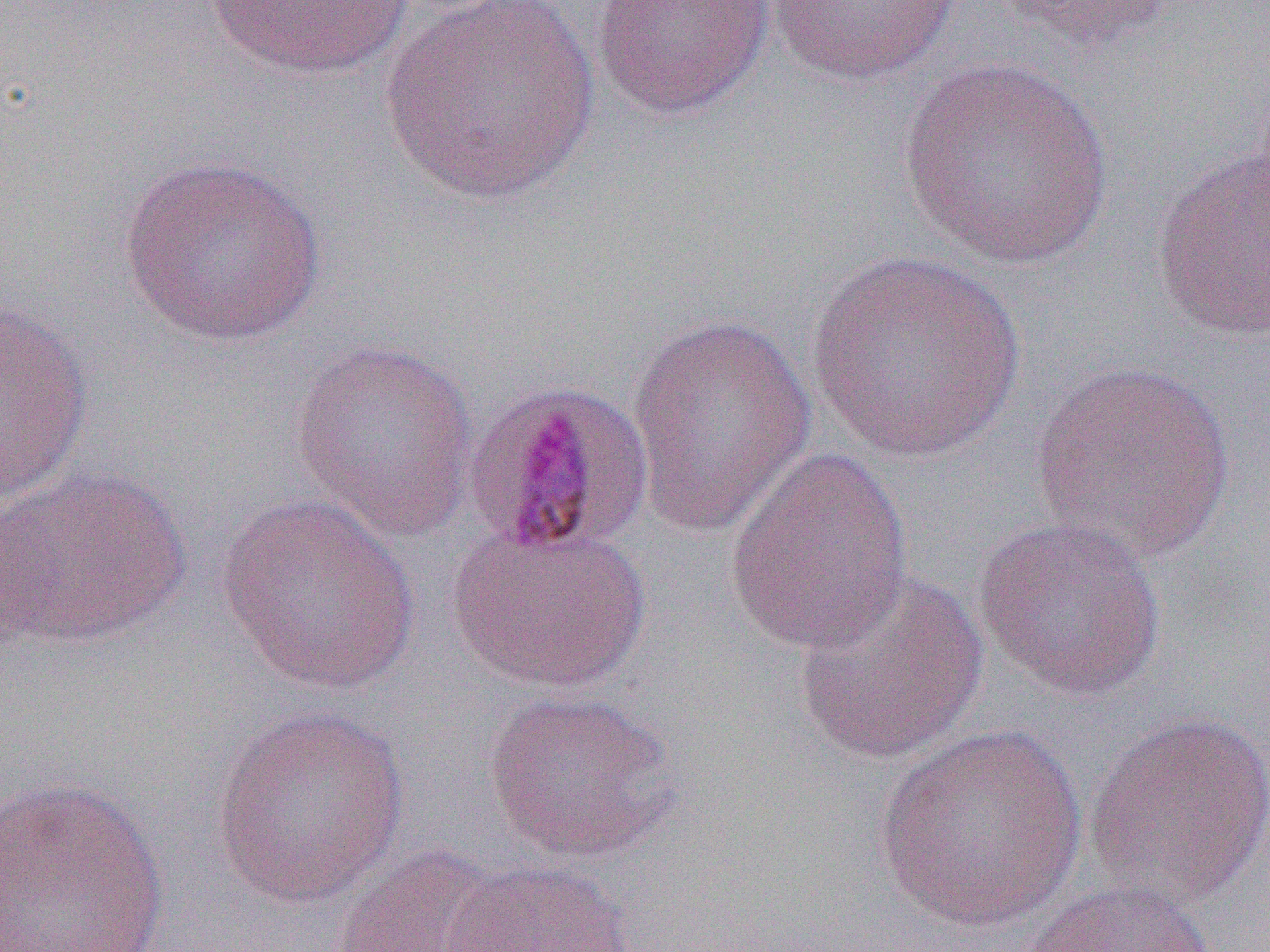
Summary:
  - Coordinate format: approximate bounding boxes as (x1,y1)-(x2,y2) corner pairs in pixels
  - Uninfected red blood cell locations: (202,0)-(420,80), (590,0)-(775,122), (986,0)-(1181,52), (377,1)-(602,205), (767,1)-(961,85), (895,57)-(1118,272), (1150,144)-(1269,342), (117,153)-(328,348), (804,250)-(1025,463), (0,301)-(94,506), (626,316)-(818,536), (288,337)-(481,541), (1029,360)-(1238,563), (725,449)-(915,655), (0,465)-(193,651), (216,493)-(422,695), (973,516)-(1168,702), (447,522)-(651,693), (790,566)-(990,766), (482,688)-(681,863), (210,705)-(411,908), (1083,708)-(1270,909), (873,722)-(1086,934), (0,775)-(170,952), (330,842)-(506,952), (441,858)-(636,952), (1015,878)-(1224,952)
  - Plasmodium malariae-infected red blood cell locations: (461,377)-(655,559)
  - Slide-level diagnosis: Plasmodium malariae
  - Magnification: 1000x
  - Preparation: thin blood film
  - Field of view: one of a larger specimen
  - Modality: light microscopy
  - Image size: 1270×952 pixels